Outline each uninfected red blood cell.
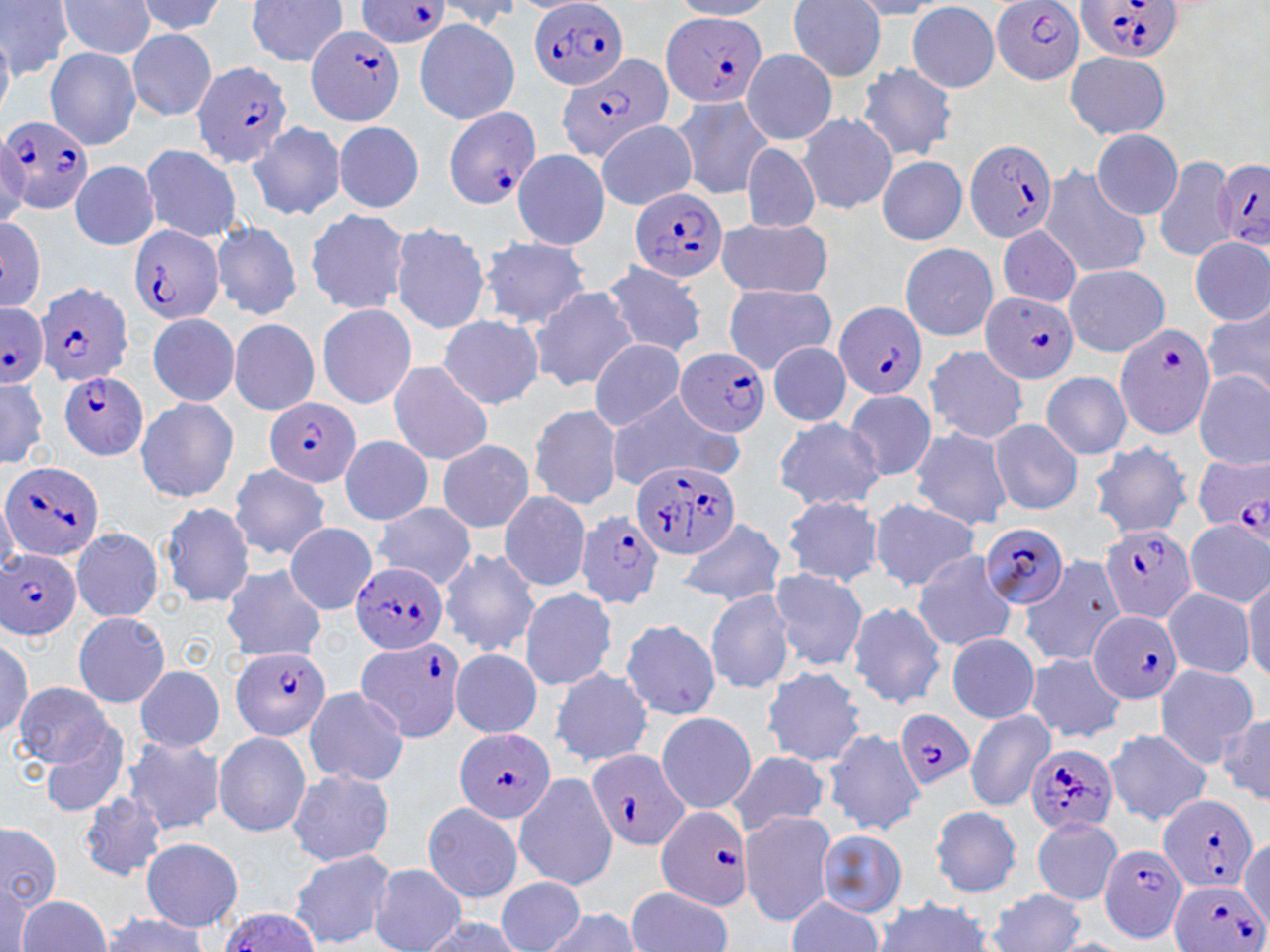

Approximate bounding boxes as [x1, y1, x2, y2] in pixels.
Uninfected red blood cells: [0, 0, 71, 79], [134, 0, 227, 37], [244, 0, 351, 68], [55, 1, 159, 60], [672, 1, 778, 19], [786, 1, 888, 80], [847, 1, 949, 19], [432, 2, 525, 33], [907, 2, 1002, 93], [414, 18, 520, 126], [125, 28, 218, 120], [0, 29, 16, 123], [45, 46, 142, 151], [741, 49, 838, 145], [1064, 49, 1173, 140], [856, 63, 958, 163], [670, 94, 773, 199], [797, 112, 897, 215], [593, 120, 697, 209], [247, 121, 346, 220], [333, 121, 425, 213], [1091, 128, 1183, 220], [740, 143, 821, 234], [138, 144, 245, 241], [512, 148, 610, 250], [1153, 154, 1236, 263], [876, 155, 968, 246], [70, 160, 159, 250], [1038, 165, 1150, 279], [304, 208, 414, 315], [0, 214, 47, 315], [714, 218, 833, 297], [210, 220, 303, 321], [389, 222, 490, 335], [997, 223, 1083, 308], [476, 236, 593, 329], [1189, 236, 1269, 325], [899, 243, 998, 341], [603, 263, 707, 358], [1062, 263, 1169, 356], [722, 284, 836, 372], [529, 286, 639, 392], [315, 303, 417, 410], [1204, 304, 1270, 400], [146, 312, 241, 407], [437, 315, 544, 409], [227, 318, 320, 416], [586, 339, 687, 432], [767, 342, 851, 426], [925, 345, 1028, 444], [385, 362, 494, 464], [1040, 370, 1133, 459], [1193, 370, 1270, 469], [0, 371, 51, 472], [607, 388, 739, 489], [844, 389, 936, 482], [133, 395, 240, 504], [528, 403, 624, 511], [772, 415, 885, 512], [987, 418, 1083, 515], [908, 425, 1015, 530], [338, 436, 436, 525], [435, 439, 536, 533], [1087, 442, 1193, 539], [228, 464, 332, 561], [498, 489, 592, 593], [780, 494, 884, 587], [0, 495, 19, 575], [161, 501, 256, 608], [868, 501, 983, 590], [370, 503, 478, 587], [677, 518, 788, 608], [1184, 519, 1269, 606], [284, 522, 376, 613], [70, 527, 164, 622], [438, 548, 541, 656], [910, 549, 1020, 651], [1019, 555, 1123, 666], [221, 564, 328, 662], [769, 567, 867, 671], [1244, 567, 1270, 683], [735, 575, 848, 722], [518, 586, 618, 690], [705, 587, 797, 694], [1163, 587, 1256, 678], [847, 600, 949, 710], [71, 612, 170, 709], [618, 619, 721, 720], [0, 632, 37, 739], [944, 632, 1041, 724], [450, 647, 542, 738], [1023, 652, 1128, 743], [1152, 663, 1260, 766], [551, 664, 653, 767], [135, 665, 225, 752], [761, 666, 865, 766], [14, 680, 114, 769], [301, 686, 410, 787], [655, 711, 757, 812], [964, 711, 1054, 811], [1217, 713, 1270, 805], [39, 722, 133, 819], [823, 728, 925, 836], [1104, 729, 1211, 825], [213, 731, 312, 838], [121, 735, 226, 836], [726, 751, 830, 836], [286, 768, 395, 866], [513, 773, 617, 889], [78, 793, 166, 882], [421, 802, 524, 903], [929, 804, 1022, 897], [738, 810, 836, 925], [1030, 816, 1123, 905], [1, 824, 63, 912], [816, 830, 907, 918], [1240, 836, 1270, 926], [140, 837, 243, 930], [288, 849, 396, 949], [369, 864, 466, 952], [495, 874, 584, 951], [0, 880, 36, 952], [624, 887, 733, 952], [988, 889, 1088, 952], [17, 895, 111, 951], [784, 896, 885, 950], [869, 898, 996, 952], [542, 907, 643, 951], [99, 911, 213, 951], [419, 916, 523, 952].

Plasmodium falciparum-infected red blood cell locations: [530, 0, 628, 92], [990, 0, 1088, 86], [1074, 0, 1184, 64], [356, 1, 454, 49], [661, 12, 768, 107], [307, 23, 407, 126], [556, 55, 674, 160], [192, 61, 295, 169], [442, 106, 541, 210], [0, 116, 96, 215], [963, 140, 1058, 245], [1214, 157, 1270, 257], [628, 188, 728, 283], [127, 223, 225, 327], [35, 281, 135, 386], [981, 290, 1078, 385], [0, 302, 48, 386], [834, 302, 927, 401], [1114, 322, 1218, 440], [676, 346, 770, 438], [59, 371, 150, 460], [265, 399, 361, 486], [1192, 452, 1270, 539], [632, 458, 741, 559], [0, 461, 108, 562], [576, 509, 666, 610], [980, 522, 1074, 606], [1101, 525, 1197, 626], [0, 548, 83, 641], [351, 560, 448, 655], [1086, 609, 1183, 705], [354, 636, 465, 743], [232, 646, 330, 742], [895, 710, 973, 790], [453, 728, 556, 824], [1025, 743, 1119, 835], [588, 750, 692, 851], [1158, 794, 1261, 895], [655, 805, 754, 912], [1097, 844, 1190, 944], [1171, 878, 1264, 952], [215, 908, 321, 952]. Slide-level diagnosis: Plasmodium falciparum. Thin blood smear. May-Grünwald-Giemsa stain. Captured at 1000x magnification. One field of a larger specimen. Light microscopy. Image is 1270×952 pixels.